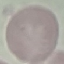
malaria status = uninfected
capture = smartphone camera at the microscope eyepiece
stain = Giemsa
image type = cell patch, automatically extracted from a larger field of view and resized to 64 × 64 pixels
preparation = thin blood film